Locate and identify every blood parasite.
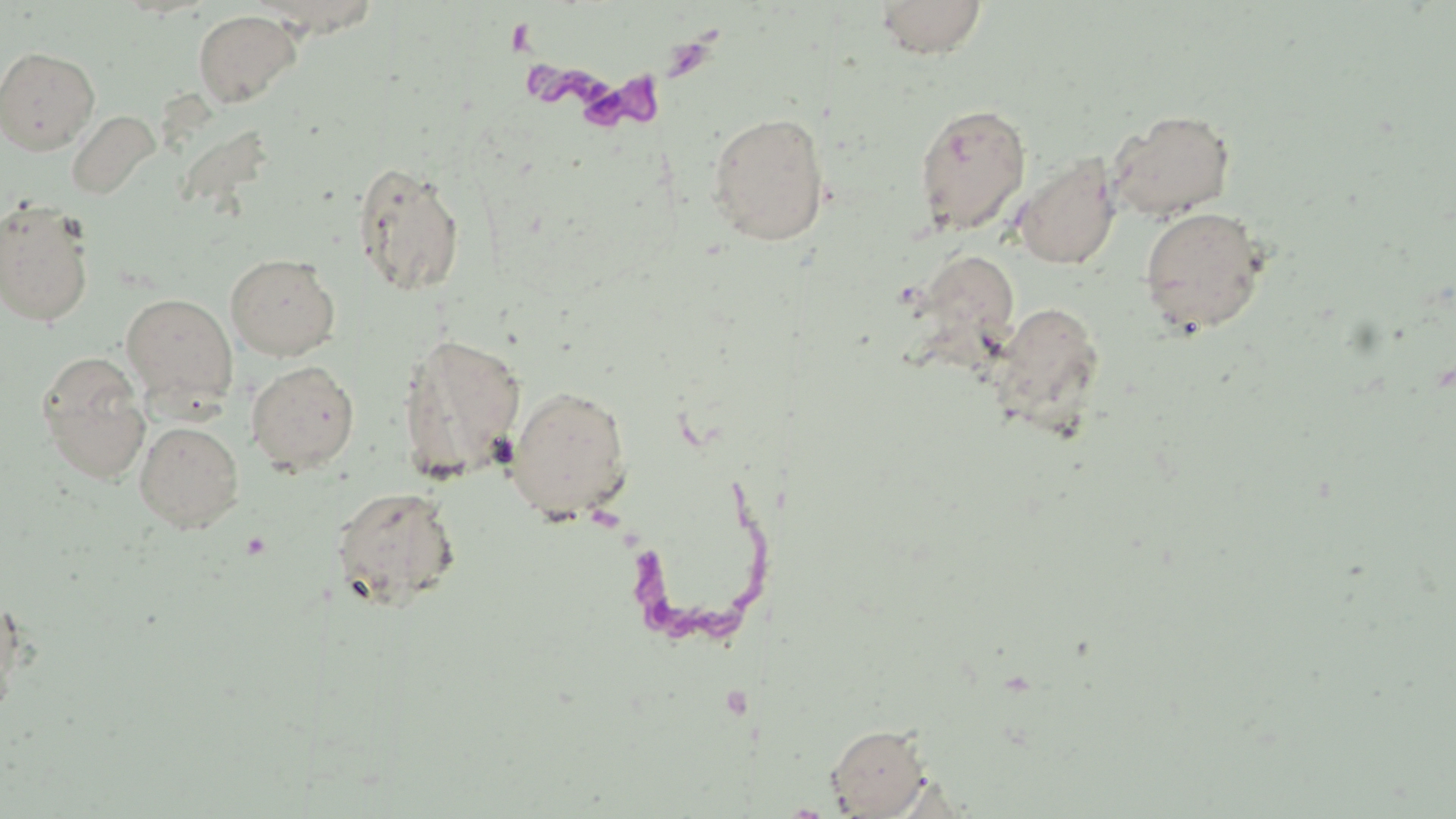
Approximate bounding boxes as (x1,y1)-(x2,y2) corner pairs in pixels.
Trypanosoma brucei: (508,23)-(739,143), (627,475)-(771,656).
No Plasmodium falciparum, Plasmodium ovale, Plasmodium malariae, Plasmodium vivax, or Babesia divergens observed.

slide-level diagnosis = Trypanosoma brucei
image size = 1456×819 pixels
uninfected red blood cell locations = approximate bounding boxes as (x1,y1)-(x2,y2) corner pairs in pixels: (873,0)-(987,59), (193,8)-(302,108), (0,45)-(100,155), (913,102)-(1032,236), (67,109)-(160,200), (1107,109)-(1237,222), (706,111)-(830,247), (1013,154)-(1121,270), (351,161)-(466,296), (0,198)-(96,328), (1138,205)-(1270,336), (920,251)-(1022,344), (225,253)-(341,360), (120,292)-(238,408), (990,302)-(1106,433), (397,333)-(527,483), (37,355)-(151,482), (245,360)-(360,474), (505,385)-(633,521), (134,420)-(244,532), (331,486)-(461,611), (0,591)-(23,725), (825,722)-(933,817)
magnification = 1000x
stain = May-Grünwald-Giemsa
modality = light microscopy
preparation = thin blood film
field of view = one of a larger specimen